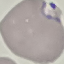

Summary:
  - Result: malaria parasites identified
  - Stain: Giemsa
  - Preparation: thin blood smear
  - Capture: smartphone camera at the microscope eyepiece
  - Image type: cell patch, automatically extracted from a larger field of view and resized to 64 × 64 pixels